Identify the parasite.
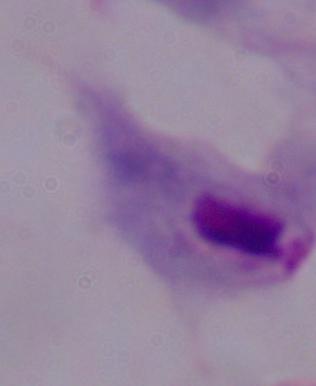
A trichomonad.

1000x magnification. Micrograph.